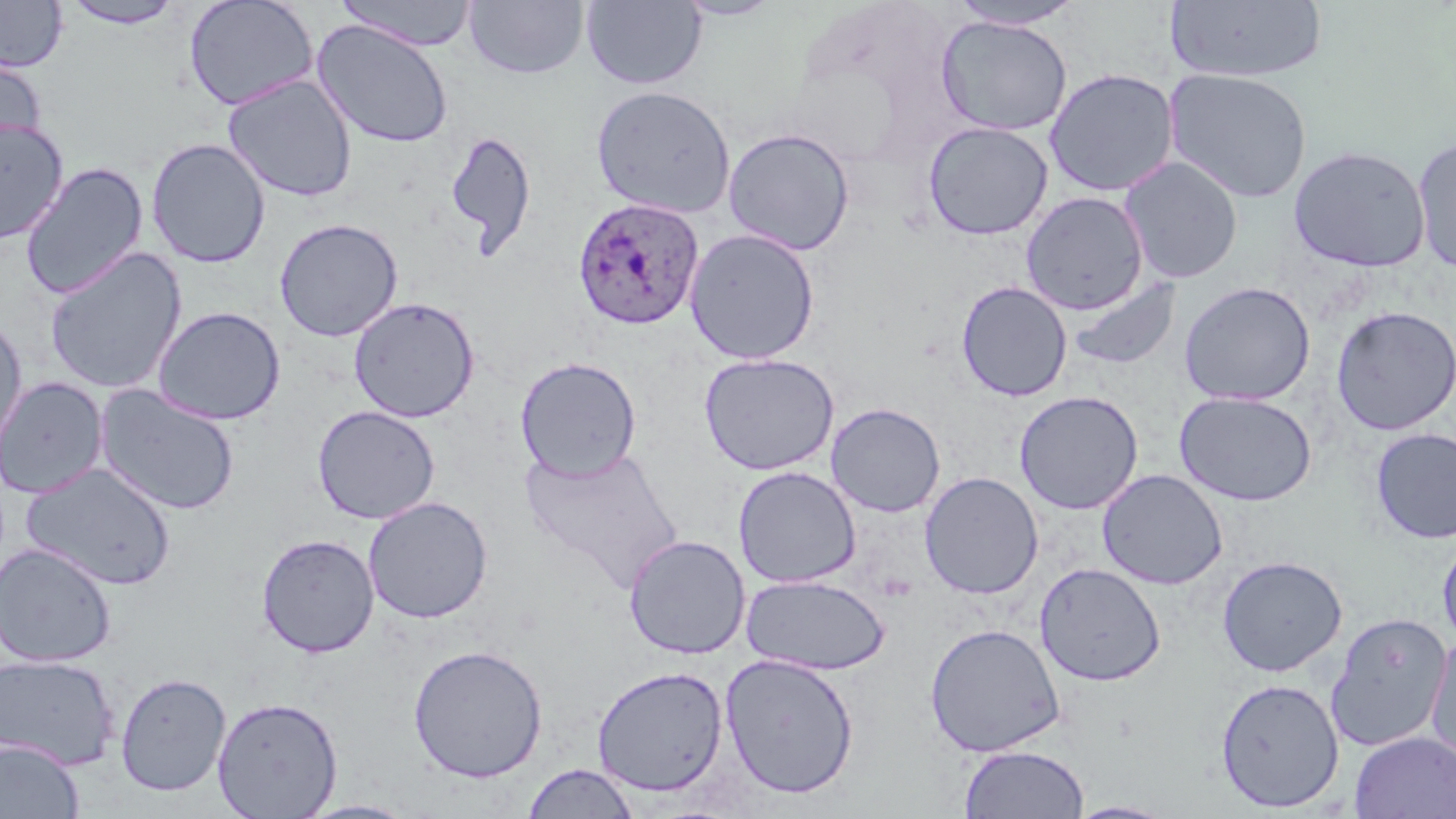

Summary:
  - Coordinate format: approximate bounding boxes as named x1/y1/x2/y2 corners in pixels
  - Uninfected red blood cell locations: (x1=184, y1=0, x2=318, y2=112), (x1=335, y1=0, x2=480, y2=51), (x1=582, y1=0, x2=706, y2=89), (x1=674, y1=0, x2=783, y2=21), (x1=0, y1=1, x2=69, y2=72), (x1=61, y1=1, x2=187, y2=29), (x1=464, y1=1, x2=589, y2=80), (x1=946, y1=1, x2=1087, y2=30), (x1=1167, y1=1, x2=1327, y2=84), (x1=935, y1=15, x2=1073, y2=137), (x1=312, y1=19, x2=453, y2=148), (x1=0, y1=52, x2=47, y2=159), (x1=1044, y1=68, x2=1180, y2=197), (x1=1163, y1=68, x2=1313, y2=203), (x1=223, y1=75, x2=358, y2=202), (x1=590, y1=85, x2=736, y2=218), (x1=0, y1=118, x2=69, y2=245), (x1=922, y1=121, x2=1054, y2=240), (x1=723, y1=127, x2=856, y2=255), (x1=444, y1=130, x2=537, y2=258), (x1=1411, y1=135, x2=1456, y2=274), (x1=146, y1=138, x2=270, y2=268), (x1=1289, y1=145, x2=1431, y2=273), (x1=1119, y1=156, x2=1243, y2=283), (x1=19, y1=161, x2=149, y2=300), (x1=1021, y1=192, x2=1149, y2=314), (x1=275, y1=218, x2=403, y2=342), (x1=684, y1=228, x2=820, y2=365), (x1=44, y1=247, x2=187, y2=395), (x1=1064, y1=275, x2=1182, y2=374), (x1=956, y1=280, x2=1072, y2=402), (x1=1179, y1=281, x2=1316, y2=406), (x1=348, y1=297, x2=480, y2=422), (x1=152, y1=306, x2=286, y2=425), (x1=1331, y1=306, x2=1456, y2=435), (x1=0, y1=314, x2=28, y2=453), (x1=698, y1=352, x2=840, y2=475), (x1=515, y1=356, x2=641, y2=481), (x1=1, y1=377, x2=108, y2=499), (x1=95, y1=384, x2=241, y2=516), (x1=1014, y1=390, x2=1144, y2=514), (x1=1174, y1=391, x2=1318, y2=506), (x1=826, y1=403, x2=945, y2=518), (x1=312, y1=405, x2=440, y2=524), (x1=1370, y1=428, x2=1456, y2=544), (x1=520, y1=445, x2=683, y2=593), (x1=21, y1=463, x2=177, y2=591), (x1=732, y1=466, x2=861, y2=588), (x1=1096, y1=469, x2=1228, y2=589), (x1=919, y1=471, x2=1043, y2=599), (x1=363, y1=496, x2=493, y2=623), (x1=618, y1=532, x2=744, y2=795), (x1=256, y1=533, x2=380, y2=657), (x1=623, y1=534, x2=750, y2=660), (x1=1437, y1=535, x2=1456, y2=651), (x1=0, y1=542, x2=117, y2=667), (x1=1217, y1=555, x2=1348, y2=677), (x1=1034, y1=562, x2=1166, y2=687), (x1=741, y1=573, x2=892, y2=676), (x1=1326, y1=612, x2=1453, y2=753), (x1=925, y1=622, x2=1066, y2=757), (x1=1425, y1=631, x2=1456, y2=766), (x1=407, y1=644, x2=548, y2=783), (x1=720, y1=653, x2=860, y2=799), (x1=0, y1=654, x2=120, y2=770), (x1=592, y1=665, x2=729, y2=797), (x1=115, y1=671, x2=232, y2=797), (x1=1214, y1=677, x2=1345, y2=813), (x1=212, y1=696, x2=343, y2=818), (x1=1350, y1=732, x2=1456, y2=819), (x1=0, y1=739, x2=84, y2=819), (x1=959, y1=744, x2=1088, y2=819), (x1=522, y1=763, x2=640, y2=819), (x1=294, y1=798, x2=421, y2=818), (x1=1065, y1=800, x2=1178, y2=818)
  - Plasmodium ovale-infected red blood cell locations: (x1=572, y1=198, x2=705, y2=330)
  - Slide-level diagnosis: Plasmodium ovale
  - Image size: 1456×819 pixels
  - Modality: optical microscopy
  - Field of view: one of a larger specimen
  - Stain: May-Grünwald-Giemsa
  - Preparation: thin blood smear
  - Magnification: 1000x